Locate and identify every blood parasite.
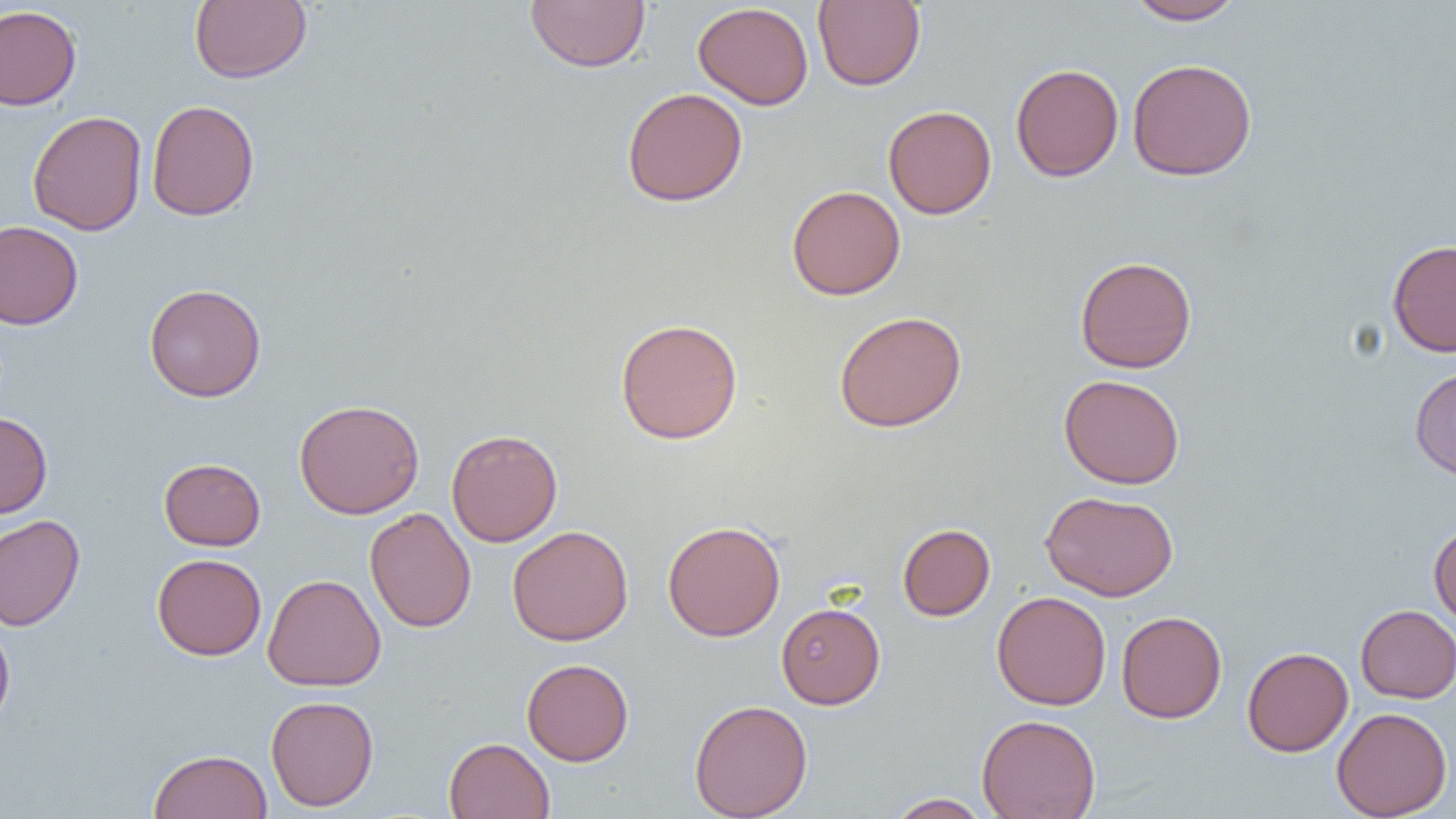
No blood parasites seen.

Approximate bounding boxes as [x1, y1, x2, y2] in pixels. Uninfected red blood cell locations: [190, 0, 312, 84], [525, 0, 651, 73], [812, 0, 926, 91], [1126, 0, 1246, 25], [693, 2, 815, 110], [0, 5, 82, 110], [1127, 58, 1257, 181], [1010, 63, 1123, 182], [622, 87, 748, 207], [146, 99, 259, 221], [883, 104, 997, 219], [27, 110, 147, 236], [786, 185, 906, 300], [0, 220, 84, 330], [1387, 240, 1456, 357], [1075, 256, 1197, 373], [144, 283, 266, 402], [834, 310, 967, 433], [615, 317, 744, 445], [1409, 367, 1456, 481], [1059, 374, 1185, 489], [293, 399, 424, 519], [0, 411, 53, 518], [446, 429, 562, 547], [159, 458, 265, 551], [1040, 490, 1178, 601], [365, 507, 476, 633], [0, 514, 85, 632], [662, 520, 785, 642], [897, 523, 995, 621], [1429, 523, 1456, 631], [507, 525, 634, 646], [152, 553, 266, 660], [263, 573, 386, 692], [992, 591, 1111, 710], [776, 602, 885, 709], [1355, 604, 1456, 703], [1116, 611, 1227, 723], [0, 619, 15, 730], [1242, 646, 1353, 756], [522, 658, 634, 766], [266, 695, 379, 811], [688, 699, 812, 818], [1332, 707, 1452, 818], [976, 713, 1101, 819], [443, 737, 555, 819], [148, 749, 272, 819], [885, 793, 993, 818]. Slide-level diagnosis: no evidence of blood parasites. Optical microscopy. One field of a larger specimen. Captured at 1000x magnification. Thin blood smear. Image is 1456×819 pixels.